Give a bounding box for every Plasmodium parasite.
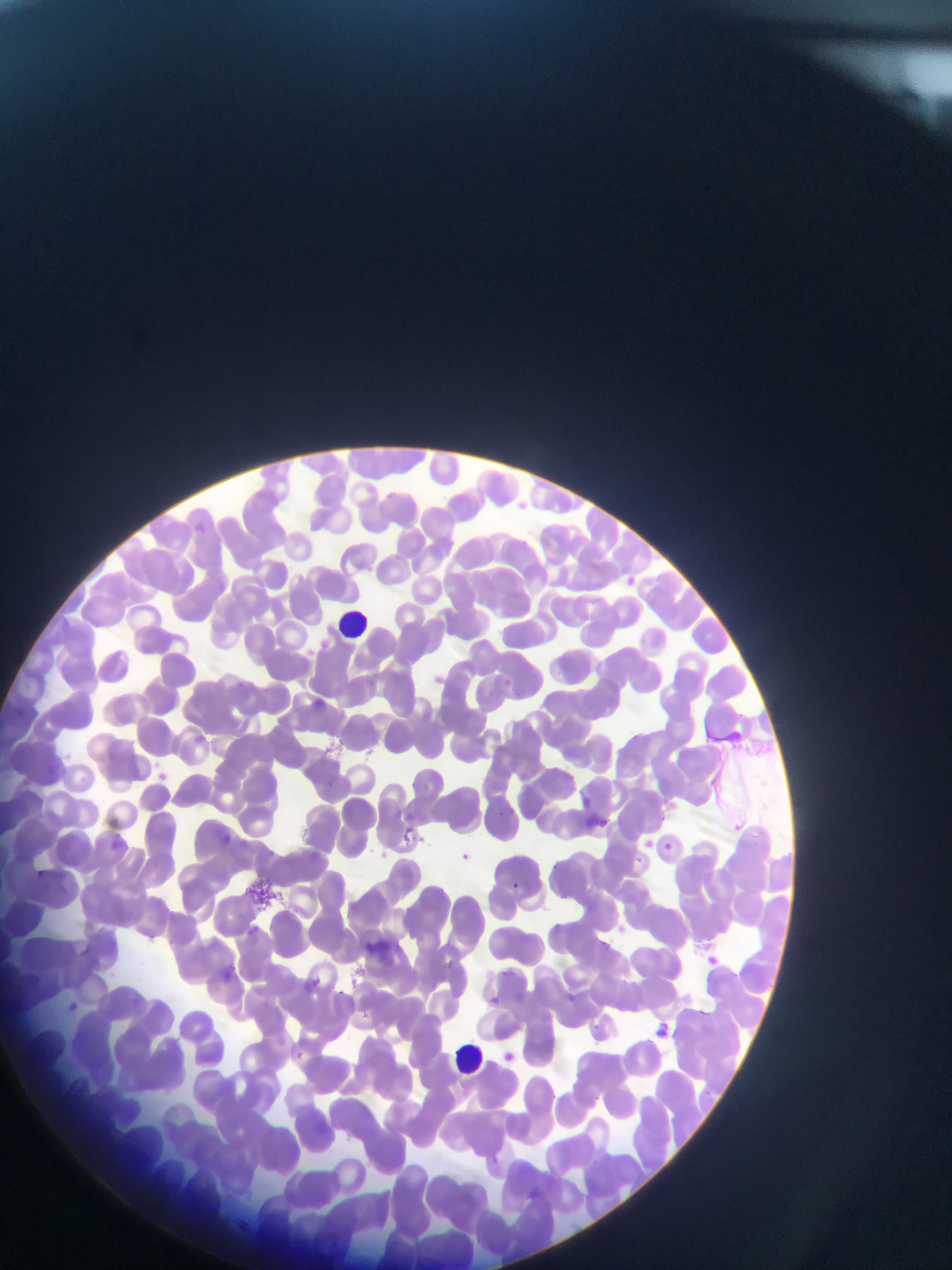

Approximate bounding boxes as (left, top, right, bottom) in pixels.
Plasmodium parasites: (623, 573, 636, 585), (231, 675, 262, 711), (310, 693, 332, 713), (581, 795, 593, 809), (497, 804, 513, 826), (405, 808, 422, 828), (599, 814, 612, 830), (398, 824, 421, 850), (213, 828, 250, 852), (643, 837, 657, 852), (117, 838, 149, 860), (660, 840, 674, 856), (455, 849, 469, 865), (36, 867, 59, 887), (511, 878, 528, 895), (548, 915, 571, 938), (77, 938, 109, 964), (705, 954, 724, 966), (213, 961, 248, 987), (313, 970, 333, 986), (560, 988, 572, 1005), (488, 993, 502, 1007), (62, 998, 88, 1015), (652, 1019, 679, 1054), (289, 1045, 303, 1063), (503, 1051, 516, 1066), (526, 1182, 544, 1214).

Leukocyte locations: (326, 600, 366, 640), (445, 1037, 495, 1087). Mobile-phone photograph taken through the microscope. Thin blood smear. Sample from Ghana. One field of view. Image is 952×1270 pixels.